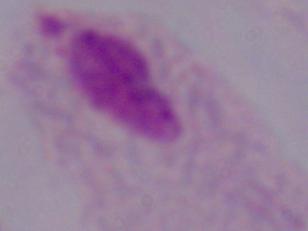
Summary:
  - Magnification: 1000x
  - Modality: photomicrograph
  - Identification: trichomonad